Locate and identify every blood parasite.
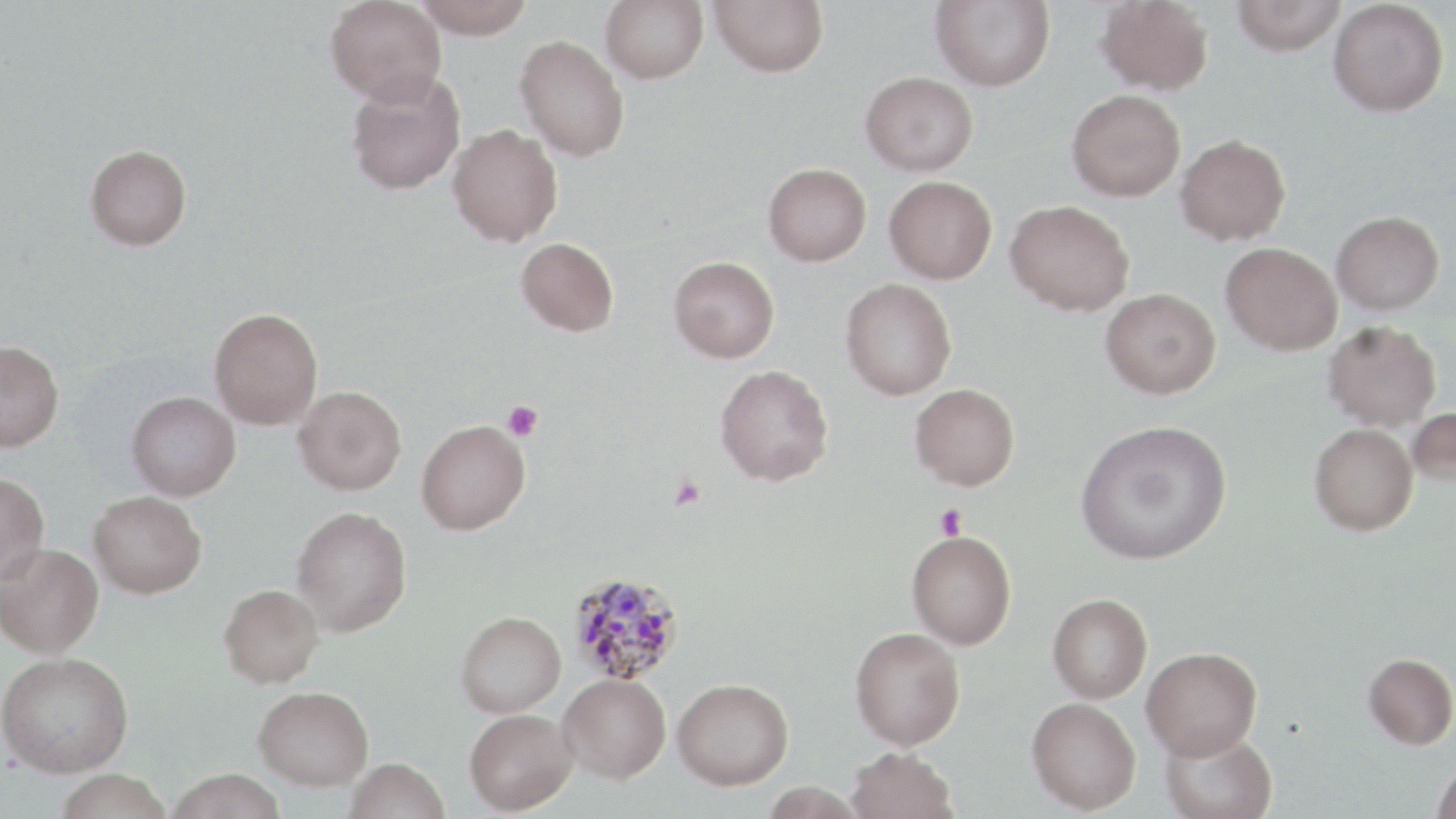
Approximate bounding boxes as (x1, y1, x2, y2) in pixels.
Plasmodium malariae-infected red blood cells: (566, 570, 685, 687).
No Plasmodium falciparum, Plasmodium ovale, Plasmodium vivax, Babesia divergens, or Trypanosoma brucei observed.

slide-level diagnosis = Plasmodium malariae
stain = May-Grünwald-Giemsa
platelet locations = approximate bounding boxes as (x1, y1, x2, y2) in pixels: (502, 400, 543, 442), (669, 476, 706, 512), (934, 504, 968, 540)
magnification = 1000x
uninfected red blood cell locations = approximate bounding boxes as (x1, y1, x2, y2) in pixels: (325, 0, 446, 106), (412, 0, 535, 39), (601, 0, 708, 84), (709, 0, 829, 77), (930, 0, 1055, 90), (1096, 0, 1214, 95), (1231, 0, 1346, 55), (1328, 1, 1448, 117), (515, 35, 629, 162), (345, 71, 466, 195), (860, 71, 978, 176), (1066, 89, 1185, 202), (447, 125, 562, 247), (1175, 134, 1290, 245), (85, 144, 192, 250), (763, 163, 871, 266), (884, 176, 997, 284), (1006, 199, 1134, 316), (1332, 211, 1444, 315), (516, 237, 618, 336), (1221, 242, 1342, 356), (668, 255, 780, 363), (840, 278, 956, 400), (1100, 288, 1221, 398), (209, 308, 323, 430), (1322, 321, 1441, 431), (0, 339, 64, 452), (715, 364, 834, 486), (910, 383, 1020, 490), (293, 386, 406, 495), (126, 391, 240, 500), (1407, 406, 1456, 488), (416, 419, 530, 535), (1075, 419, 1232, 565), (1309, 423, 1418, 535), (0, 472, 49, 585), (88, 490, 206, 598), (291, 506, 412, 636), (907, 530, 1016, 650), (0, 543, 103, 658), (219, 584, 323, 687), (1048, 593, 1152, 703), (456, 611, 566, 717), (850, 626, 966, 750), (1141, 647, 1263, 760), (0, 652, 133, 776), (1363, 653, 1456, 749), (558, 674, 670, 783), (672, 677, 793, 789), (253, 686, 374, 790), (1026, 697, 1141, 813), (464, 708, 578, 814), (1159, 728, 1277, 819), (847, 746, 957, 819), (344, 757, 451, 819), (1430, 761, 1456, 819), (165, 768, 288, 819), (53, 769, 173, 819)
field of view = single
modality = optical microscopy
image size = 1456×819 pixels
preparation = thin blood film